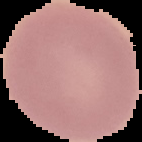

Result: no Plasmodium parasites detected. The area outside the segmented cell region is set to black. From a thin blood film. Image is 142×142 pixels.